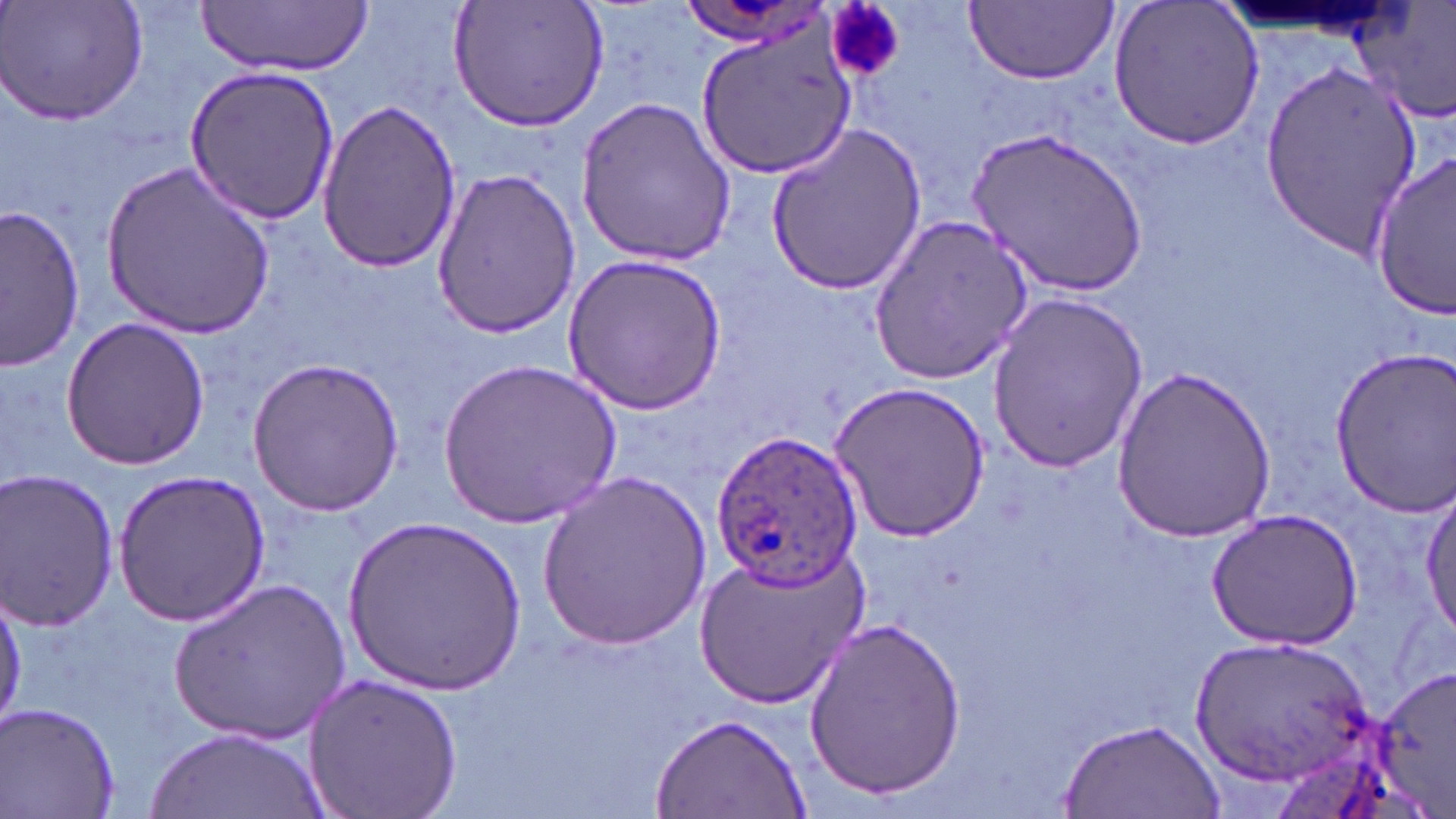

slide-level diagnosis = Plasmodium ovale
field of view = single
modality = optical microscopy
preparation = thin blood film
stain = May-Grünwald-Giemsa
magnification = 1000x
Plasmodium ovale-infected red blood cell locations = approximate bounding boxes as (x1,y1)-(x2,y2) corner pairs in pixels: (708,431)-(864,590)
platelet locations = approximate bounding boxes as (x1,y1)-(x2,y2) corner pairs in pixels: (828,3)-(906,82)
uninfected red blood cell locations = approximate bounding boxes as (x1,y1)-(x2,y2) corner pairs in pixels: (2,0)-(151,127), (198,0)-(374,75), (449,0)-(609,130), (963,1)-(1119,85), (1107,1)-(1266,152), (1354,3)-(1456,124), (694,23)-(857,177), (1259,59)-(1424,252), (183,63)-(340,226), (575,92)-(738,266), (317,100)-(462,270), (764,124)-(927,296), (973,124)-(1149,300), (1370,149)-(1456,319), (102,159)-(275,338), (428,170)-(584,337), (2,205)-(86,369), (868,213)-(1036,383), (558,252)-(731,417), (986,292)-(1147,473), (61,317)-(210,470), (1326,349)-(1456,514), (244,356)-(409,517), (441,359)-(621,527), (1110,368)-(1281,540), (830,379)-(991,544), (536,466)-(712,653), (0,469)-(121,630), (113,470)-(270,627), (1418,489)-(1455,644), (1204,508)-(1364,648), (345,515)-(525,698), (694,544)-(866,709), (171,576)-(351,743), (0,582)-(24,729), (802,615)-(965,800), (1195,633)-(1374,786), (1376,665)-(1456,813), (300,670)-(464,819), (2,703)-(121,818), (648,712)-(811,819), (1057,717)-(1225,818), (145,726)-(325,818)
image size = 1456×819 pixels